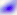

magnification = 400x
identification = Toxoplasma gondii
modality = micrograph